Name the parasite shown.
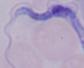
This is a trypanosome.

Summary:
  - Modality: micrograph
  - Magnification: 1000x